State which parasite is depicted.
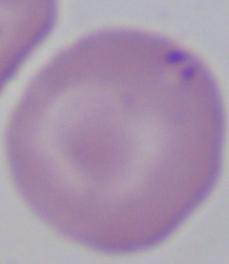

This is Babesia.

Summary:
  - Modality: micrograph
  - Magnification: 1000x